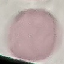

Summary:
  - Result: no malaria parasites detected
  - Capture: smartphone camera at the microscope eyepiece
  - Preparation: thin smear
  - Image type: cell patch, automatically extracted from a larger field of view and resized to 64 × 64 pixels
  - Stain: Giemsa